State which parasite is depicted.
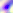

This is Toxoplasma gondii.

Photomicrograph. 400x magnification.